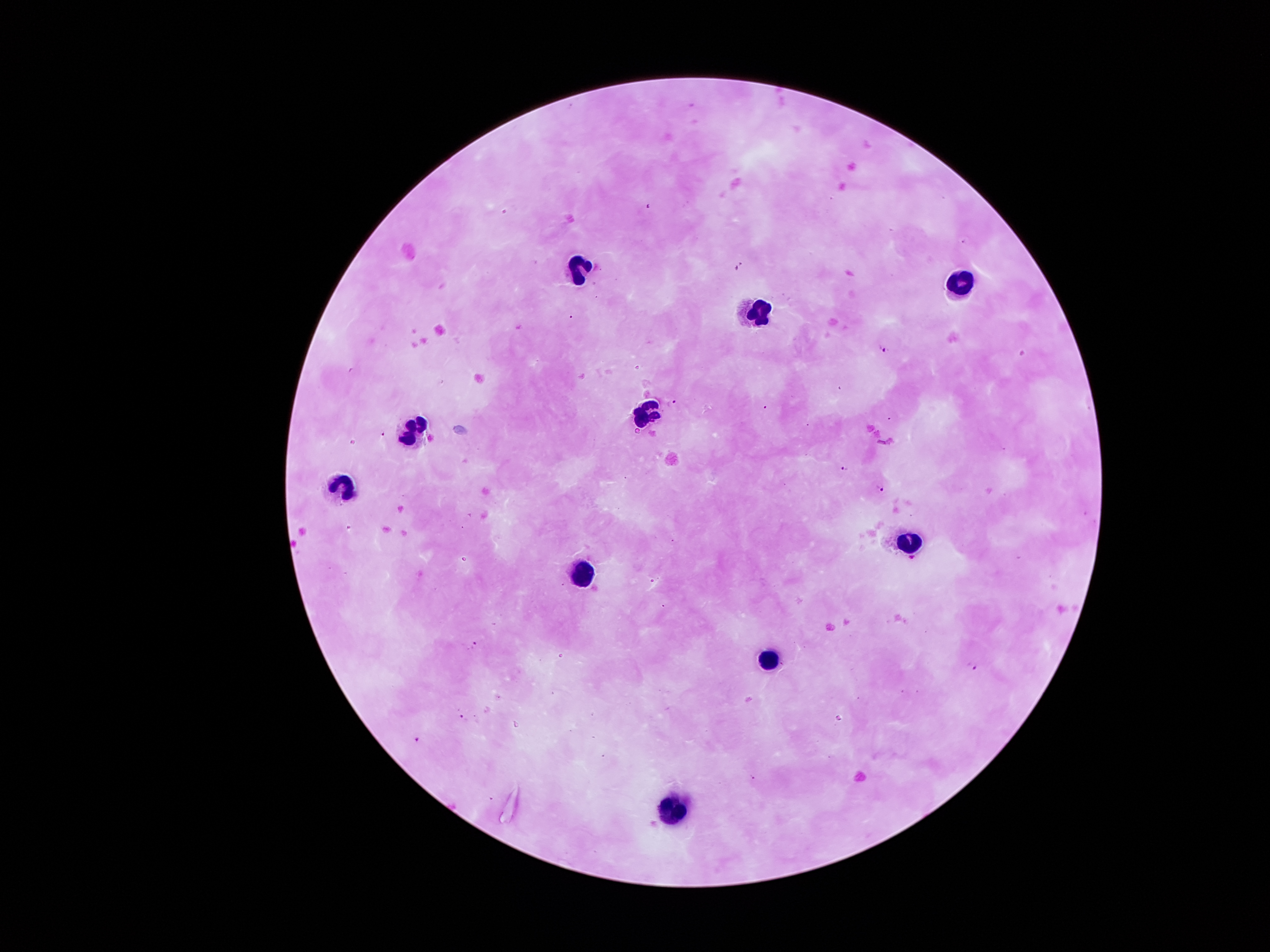
coordinate format = approximate centers as (x, y) in pixels
leukocyte locations = (577, 266), (961, 276), (758, 313), (646, 414), (414, 431), (341, 484), (908, 541), (580, 575), (772, 659), (677, 807)
malaria parasite locations = (884, 349), (671, 403), (845, 468), (880, 489), (474, 645), (973, 668), (463, 717), (418, 740), (754, 778)
stain = Giemsa
capture = smartphone camera through the microscope eyepiece
field of view = one from this slide
preparation = thick blood film
image size = 1270×952 pixels
patient malaria status = infected with Plasmodium falciparum
magnification = 100x